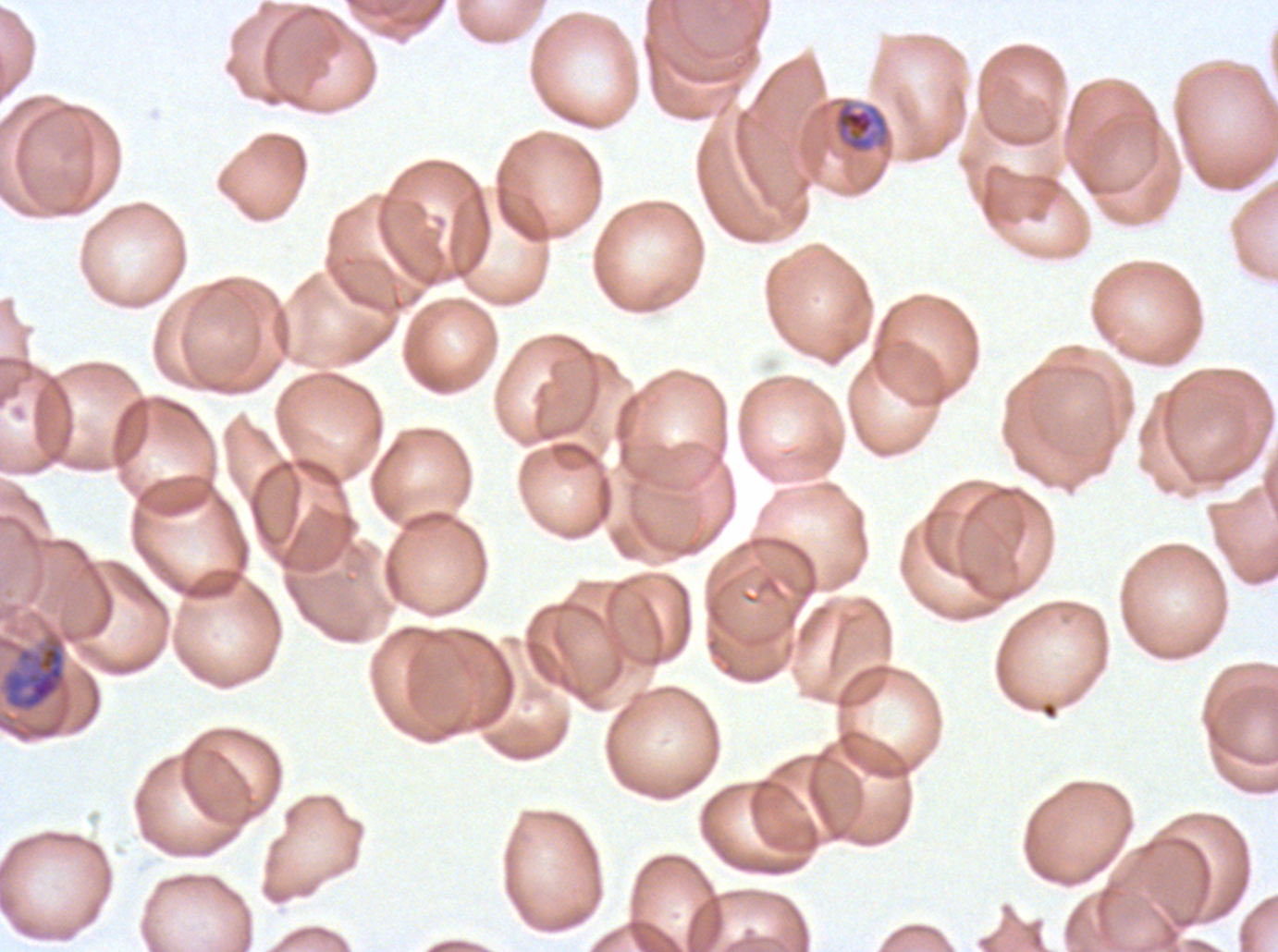
notation = approximate bounding boxes as [x1, y1, x2, y2] in pixels
late trophozoite locations = [0, 631, 68, 714]
late-ring/early-trophozoite locations = [833, 101, 890, 153]
specimen = P. falciparum from a patient in The Gambia, cultured ex vivo for 24 to 48 hours
preparation = thin blood smear
field of view = one sub-image of a larger composite
image size = 1278×952 pixels
stain = Giemsa
life-cycle stages observed = late-ring/early-trophozoite, late trophozoite